Report the malaria status of this cell.
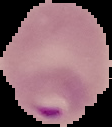

Parasitized.

Image is 112×127 pixels. From a thin blood smear. The area outside the segmented cell region is set to black.